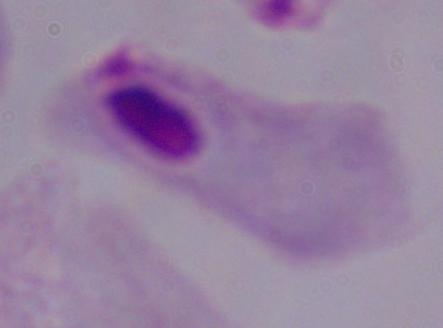
1000x magnification. Micrograph. A trichomonad is shown.